Locate every uninfected red blood cell.
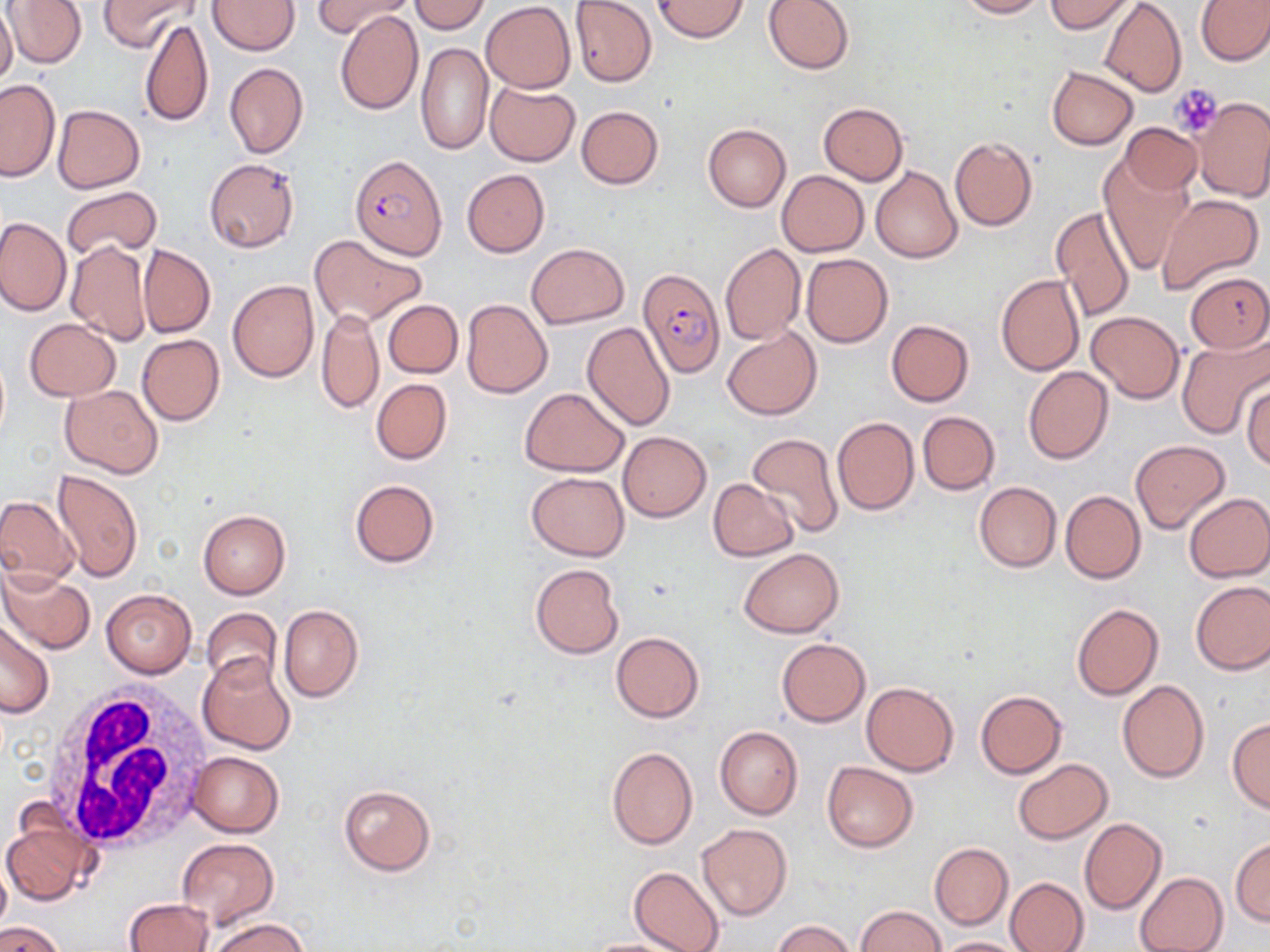
Approximate bounding boxes as (x1, y1, x2, y2) in pixels.
Uninfected red blood cells: (5, 0, 88, 67), (99, 0, 200, 52), (408, 0, 490, 33), (763, 0, 855, 75), (956, 0, 1049, 18), (1044, 0, 1136, 33), (1196, 0, 1270, 66), (208, 1, 299, 55), (317, 1, 412, 39), (481, 1, 575, 92), (570, 1, 658, 87), (653, 1, 750, 41), (1100, 1, 1187, 97), (0, 6, 18, 85), (335, 11, 423, 115), (140, 17, 214, 130), (416, 43, 493, 155), (224, 63, 308, 158), (1047, 66, 1138, 150), (0, 79, 59, 181), (484, 81, 580, 166), (1193, 97, 1270, 201), (818, 102, 908, 185), (53, 104, 145, 192), (575, 106, 664, 189), (1120, 122, 1202, 195), (702, 124, 791, 213), (949, 136, 1037, 231), (1098, 157, 1195, 276), (204, 158, 299, 253), (871, 167, 963, 263), (462, 170, 550, 257), (777, 170, 868, 256), (61, 185, 161, 258), (1158, 194, 1263, 293), (1051, 205, 1136, 322), (0, 216, 71, 315), (309, 234, 429, 327), (64, 239, 151, 346), (720, 241, 806, 346), (139, 243, 216, 337), (527, 243, 628, 328), (801, 253, 893, 348), (1185, 271, 1270, 353), (995, 273, 1084, 376), (227, 280, 319, 382), (460, 297, 553, 398), (384, 300, 463, 378), (316, 308, 383, 414), (1086, 311, 1185, 403), (24, 318, 121, 400), (886, 320, 973, 406), (581, 322, 676, 429), (722, 326, 820, 421), (136, 333, 225, 426), (1176, 336, 1270, 440), (1024, 366, 1113, 466), (371, 378, 452, 465), (1243, 381, 1270, 471), (61, 384, 162, 478), (520, 387, 629, 477), (917, 410, 999, 495), (833, 416, 919, 515), (618, 431, 711, 521), (748, 431, 844, 538), (1131, 439, 1230, 534), (53, 470, 144, 582), (526, 471, 629, 561), (349, 479, 440, 568), (708, 479, 798, 561), (974, 482, 1060, 572), (1060, 490, 1145, 583), (1183, 492, 1270, 581), (0, 495, 80, 587), (198, 508, 290, 599), (739, 548, 843, 637), (530, 562, 625, 660), (0, 567, 94, 654), (1190, 581, 1270, 674), (99, 588, 197, 678), (1071, 603, 1162, 701), (279, 605, 363, 702), (201, 608, 282, 690), (0, 618, 54, 718), (611, 631, 704, 723), (777, 638, 869, 726), (197, 653, 298, 755), (1117, 679, 1209, 785), (861, 682, 958, 775), (976, 690, 1067, 778), (1226, 717, 1270, 813), (715, 726, 802, 820), (607, 746, 698, 849), (186, 751, 284, 836), (1013, 757, 1111, 843), (822, 761, 918, 852), (338, 784, 436, 876), (2, 815, 94, 908), (1080, 817, 1166, 914), (696, 823, 792, 921), (176, 837, 280, 930), (1230, 838, 1270, 925), (930, 843, 1013, 929), (0, 860, 11, 937), (628, 866, 725, 952), (1135, 872, 1228, 952), (1005, 877, 1089, 952), (122, 899, 213, 952), (854, 906, 945, 951), (208, 917, 310, 952), (771, 920, 857, 952), (0, 922, 66, 952), (936, 936, 1027, 951), (578, 937, 699, 952).

slide-level diagnosis = Plasmodium falciparum
magnification = 1000x
stain = May-Grünwald-Giemsa
image size = 1270×952 pixels
platelet locations = approximate bounding boxes as (x1, y1, x2, y2) in pixels: (1169, 83, 1223, 138)
field of view = single
Plasmodium falciparum-infected red blood cell locations = approximate bounding boxes as (x1, y1, x2, y2) in pixels: (352, 156, 446, 262), (638, 267, 725, 377)
white blood cell locations = approximate bounding boxes as (x1, y1, x2, y2) in pixels: (43, 685, 216, 854)
modality = optical microscopy
preparation = thin blood film